Name the parasite shown.
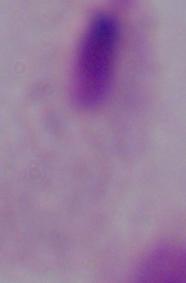
This is a trichomonad.

1000x magnification. Micrograph.